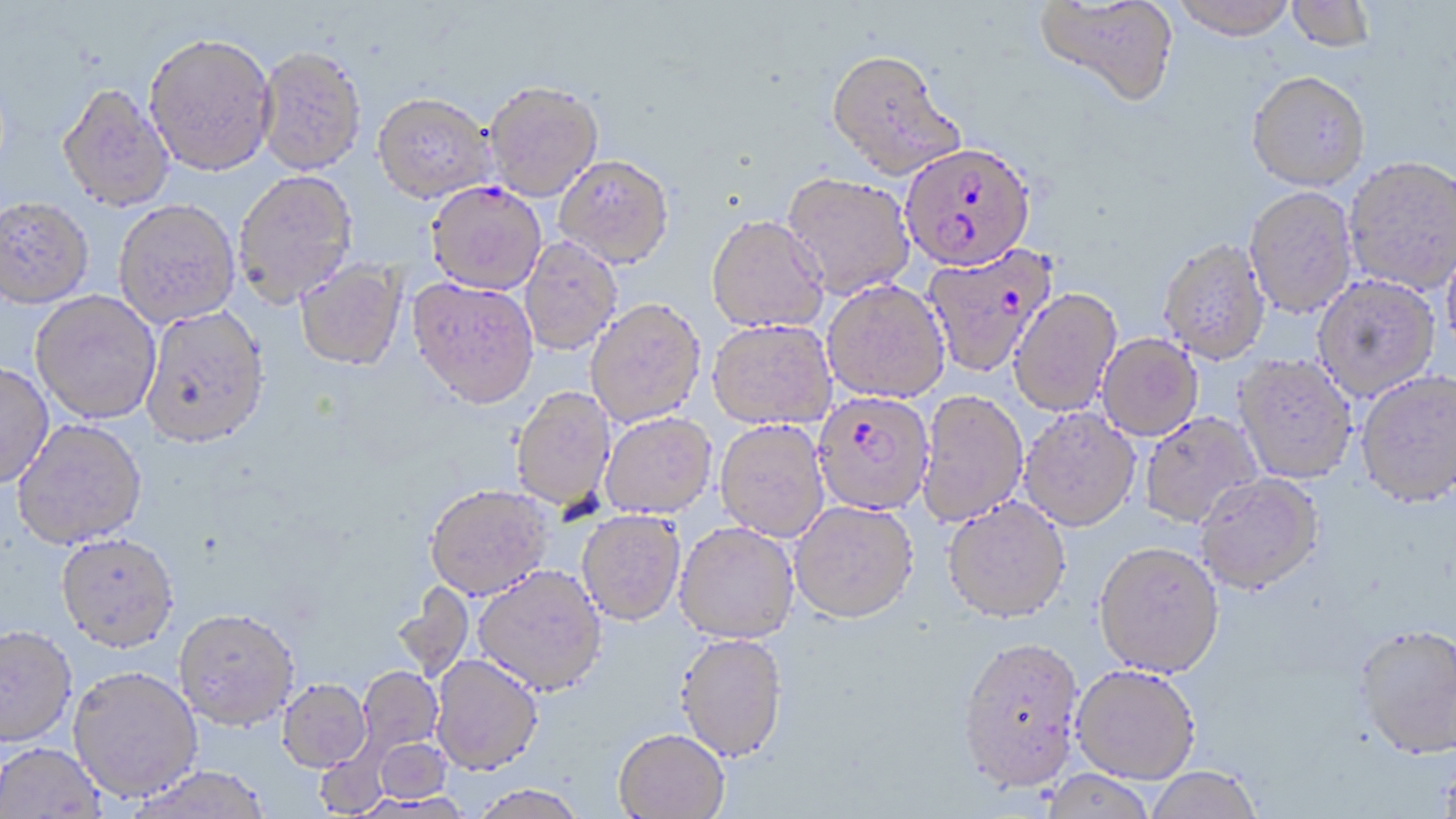
Summary:
  - Coordinate format: approximate bounding boxes as (x1,y1)-(x2,y2) corner pairs in pixels
  - Plasmodium falciparum-infected red blood cell locations: (900,142)-(1036,271), (922,244)-(1057,378), (812,390)-(935,515)
  - Uninfected red blood cell locations: (1034,0)-(1178,109), (1171,0)-(1298,41), (1286,0)-(1376,53), (144,33)-(277,177), (256,47)-(368,176), (825,50)-(965,181), (1246,71)-(1370,192), (484,80)-(604,201), (56,83)-(175,212), (371,93)-(495,204), (554,154)-(674,267), (1344,156)-(1456,296), (233,170)-(358,307), (782,171)-(916,300), (426,181)-(546,294), (1244,186)-(1358,319), (0,196)-(94,309), (114,200)-(240,328), (706,214)-(829,333), (519,236)-(623,355), (1441,238)-(1456,359), (1158,239)-(1270,364), (294,260)-(406,372), (1312,275)-(1441,402), (408,277)-(539,409), (822,279)-(950,403), (1009,287)-(1122,417), (30,290)-(161,424), (585,297)-(707,427), (140,305)-(270,449), (707,318)-(837,429), (1097,333)-(1203,441), (1234,354)-(1357,484), (0,361)-(54,489), (1356,372)-(1456,509), (511,386)-(616,510), (917,390)-(1029,527), (1019,408)-(1140,531), (1139,411)-(1262,528), (600,412)-(717,518), (12,418)-(147,549), (714,419)-(830,541), (1195,472)-(1325,595), (424,484)-(553,600), (942,496)-(1071,622), (789,500)-(918,623), (577,509)-(686,625), (675,522)-(799,643), (56,532)-(179,652), (1093,541)-(1225,677), (473,564)-(607,696), (391,582)-(475,682), (174,607)-(300,730), (0,625)-(78,748), (1354,626)-(1456,762), (675,633)-(788,761), (957,635)-(1087,792), (430,654)-(543,775), (1070,664)-(1201,784), (67,666)-(203,802), (356,666)-(445,762), (277,679)-(371,772), (613,728)-(729,819), (373,737)-(451,804), (1,742)-(106,818), (127,766)-(272,819), (1143,766)-(1264,819), (1039,770)-(1158,819), (469,783)-(589,818)
  - Slide-level diagnosis: Plasmodium falciparum
  - Modality: optical microscopy
  - Preparation: thin blood film
  - Field of view: one of a larger specimen
  - Image size: 1456×819 pixels
  - Magnification: 1000x
  - Stain: May-Grünwald-Giemsa